Assess the morphology of the erythrocytes.
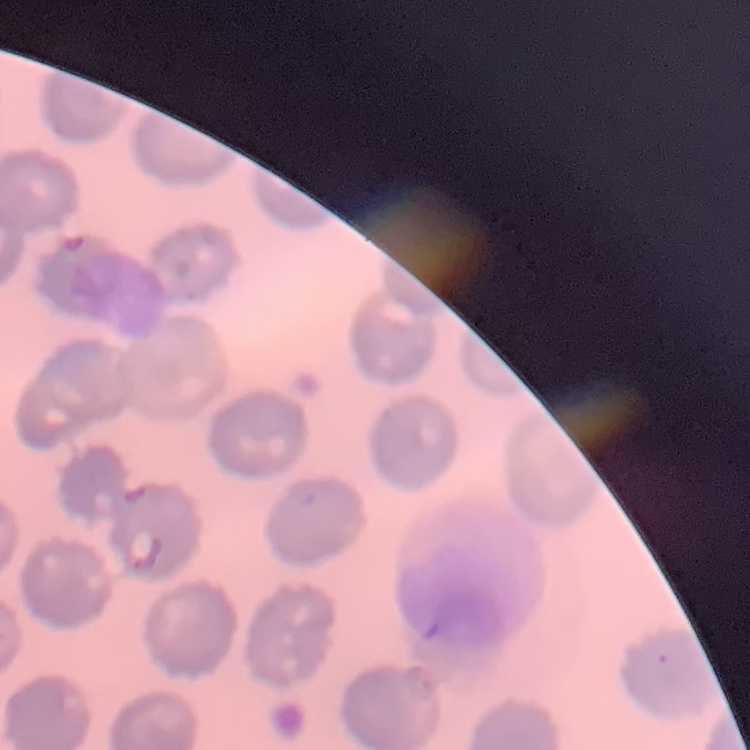
No rouleaux formation.

Summary:
  - Stain: Field's or Giemsa
  - Image type: square crop of a larger photomicrograph
  - Preparation: thin blood smear